Report the malaria status of this cell.
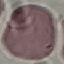

Uninfected.

Giemsa-stained preparation. Photographed with a smartphone camera at the microscope eyepiece. Thin blood smear. Automatically extracted cell patch, resized to 64 × 64 pixels.